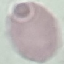

Summary:
  - Result: no malaria parasites detected
  - Image type: automatically extracted cell patch, resized to 64 × 64 pixels
  - Capture: smartphone camera at the microscope eyepiece
  - Preparation: thin blood smear
  - Stain: Giemsa